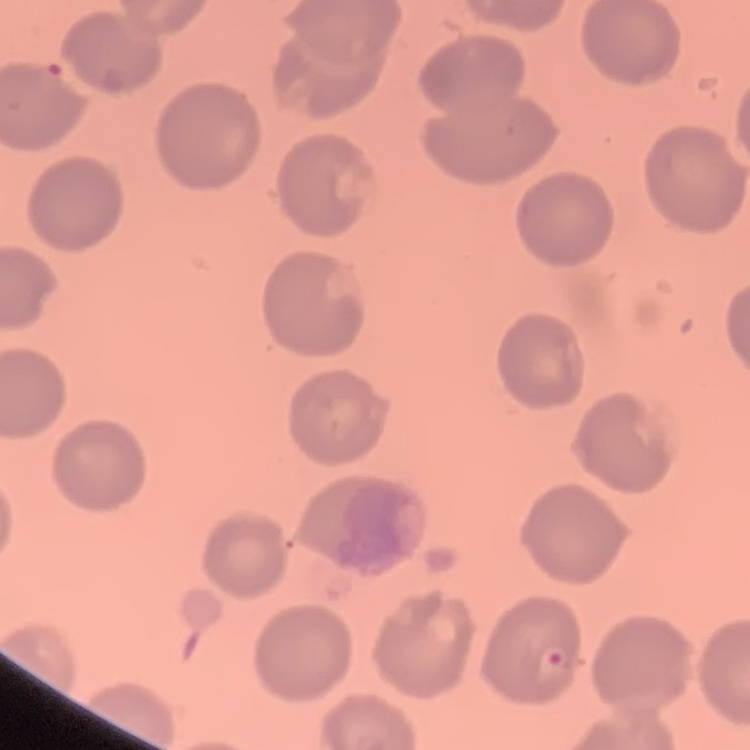
erythrocyte_morphology: no rouleaux formation
image_type: square crop of a larger photomicrograph
stain: Field's or Giemsa
preparation: thin blood smear